State which parasite is depicted.
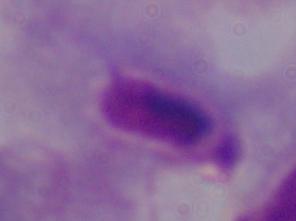
This is a trichomonad.

Summary:
  - Modality: photomicrograph
  - Magnification: 1000x